Identify the parasite.
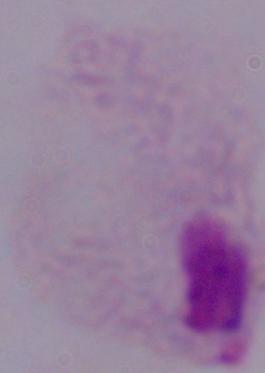
This is a trichomonad.

1000x magnification. Photomicrograph.